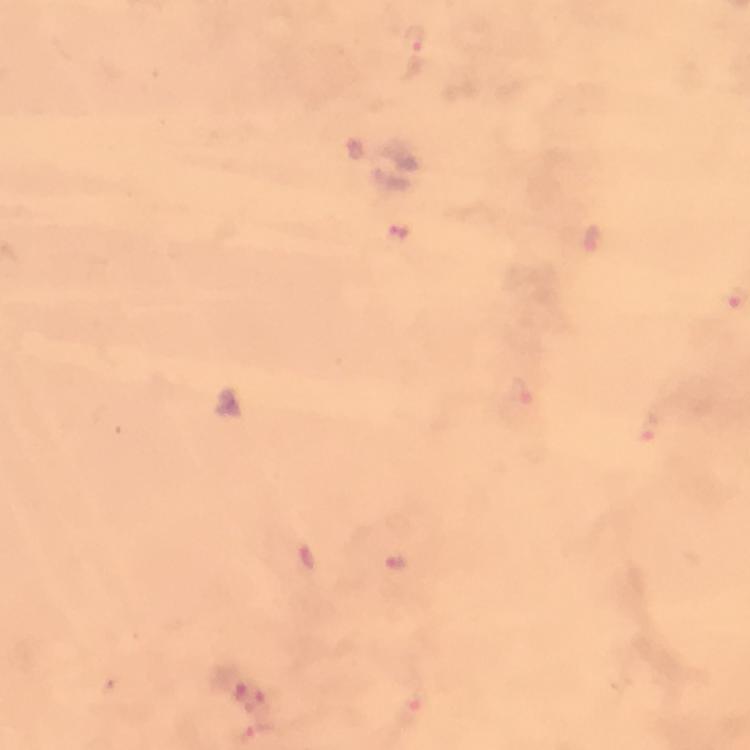

Approximate centers as [x, y] in pixels. Malaria parasite locations: [414, 54], [401, 233], [591, 239], [520, 393], [648, 428], [307, 558], [396, 561], [248, 698], [415, 707]. From a diagnostic examination for malaria. At 100x magnification. Giemsa-stained preparation. Cropped region of a single field of view. Image is 750×750 pixels. Immersion oil was used. Smartphone photograph taken through a microscope. Thick blood film.